Name the parasite shown.
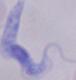

This is a trypanosome.

Summary:
  - Modality: photomicrograph
  - Magnification: 1000x